Name the cell type shown.
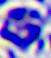

This is a leukocyte.

400x magnification. Micrograph.